Give the extent of all white blood cells.
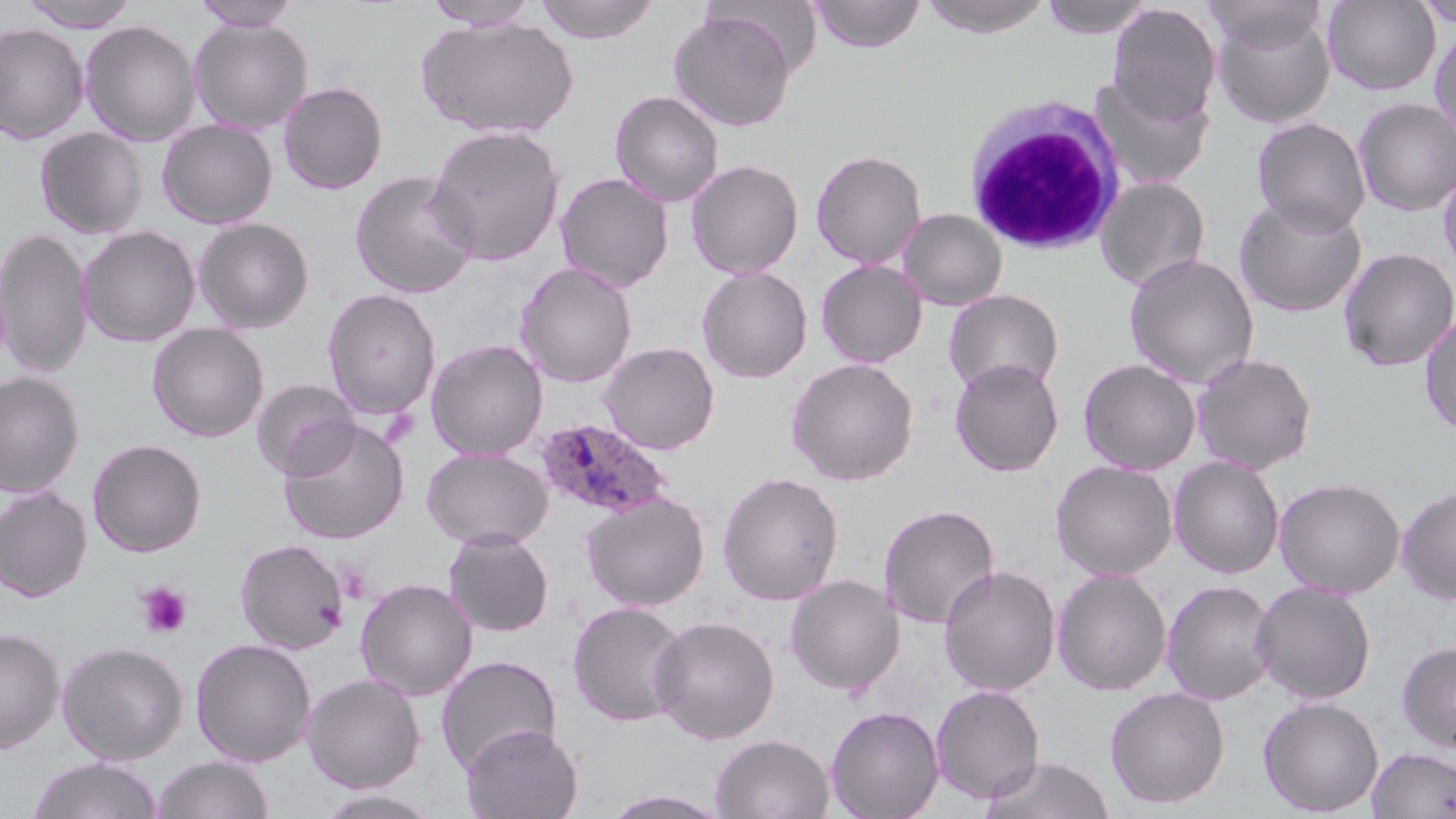
Approximate bounding boxes as (x1, y1, x2, y2) in pixels.
White blood cells: (962, 95, 1127, 255).

Summary:
  - Uninfected red blood cell locations: (18, 0, 140, 31), (535, 0, 659, 43), (807, 0, 926, 53), (915, 0, 1056, 38), (1039, 0, 1156, 39), (1205, 0, 1327, 55), (1323, 0, 1441, 95), (191, 1, 300, 31), (422, 1, 540, 31), (1413, 1, 1456, 29), (1106, 3, 1221, 124), (668, 9, 797, 132), (1211, 11, 1335, 128), (416, 15, 579, 139), (188, 19, 313, 134), (79, 20, 201, 146), (0, 22, 90, 144), (1429, 25, 1456, 143), (1090, 75, 1214, 189), (278, 81, 388, 194), (610, 90, 724, 207), (1353, 98, 1456, 216), (1251, 116, 1372, 236), (157, 119, 278, 229), (426, 123, 566, 266), (34, 127, 148, 238), (810, 149, 927, 270), (685, 159, 804, 279), (1438, 163, 1456, 280), (349, 169, 480, 299), (555, 172, 674, 293), (1095, 176, 1211, 291), (1233, 196, 1367, 317), (897, 208, 1008, 311), (193, 217, 315, 333), (77, 225, 201, 347), (0, 227, 93, 377), (1337, 247, 1456, 372), (1124, 253, 1260, 389), (815, 259, 927, 368), (515, 261, 637, 388), (697, 266, 813, 383), (321, 288, 441, 420), (943, 289, 1064, 397), (1419, 311, 1456, 437), (147, 323, 269, 442), (426, 338, 549, 460), (600, 341, 721, 454), (1190, 352, 1317, 475), (786, 358, 919, 485), (949, 358, 1064, 476), (1077, 358, 1202, 475), (0, 371, 84, 498), (252, 378, 360, 480), (278, 418, 410, 545), (87, 438, 207, 557), (421, 447, 554, 550), (1168, 454, 1285, 579), (1050, 460, 1177, 580), (717, 471, 844, 605), (1274, 477, 1406, 598), (1396, 484, 1456, 605), (0, 487, 92, 601), (581, 491, 710, 611), (878, 504, 1001, 630), (442, 529, 555, 637), (234, 538, 350, 654), (939, 565, 1060, 696), (1052, 568, 1173, 695), (786, 574, 904, 695), (355, 577, 478, 701), (1161, 579, 1278, 705), (1251, 580, 1377, 703), (568, 600, 689, 727), (648, 615, 779, 744), (0, 626, 64, 754), (190, 637, 318, 766), (1395, 640, 1456, 752), (57, 641, 188, 763), (435, 654, 562, 775), (302, 673, 426, 792), (930, 684, 1046, 804), (1104, 686, 1231, 808), (1258, 696, 1384, 816), (825, 704, 944, 819), (461, 724, 583, 819), (711, 734, 834, 818), (1367, 746, 1456, 818), (980, 754, 1115, 819), (152, 755, 274, 818), (26, 756, 165, 818), (311, 788, 447, 818), (602, 789, 734, 818)
  - Plasmodium ovale-infected red blood cell locations: (535, 418, 672, 519)
  - Platelet locations: (135, 581, 193, 639)
  - Slide-level diagnosis: Plasmodium ovale
  - Stain: May-Grünwald-Giemsa
  - Modality: light microscopy
  - Field of view: one of a larger specimen
  - Image size: 1456×819 pixels
  - Preparation: thin blood smear
  - Magnification: 1000x